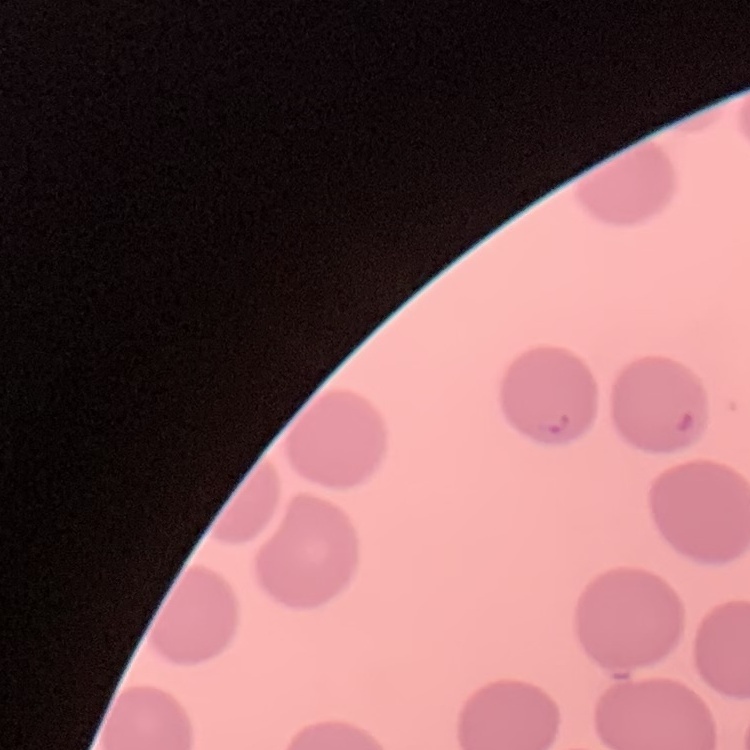

erythrocyte morphology = no rouleaux formation
preparation = thin blood smear
stain = Field's or Giemsa
image type = one tile cut from a larger photomicrograph